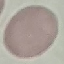
result = negative for malaria parasites
image type = cell patch, automatically extracted from a larger field of view and resized to 64 × 64 pixels
preparation = thin smear
capture = smartphone camera at the microscope eyepiece
stain = Giemsa